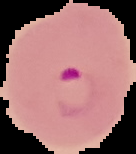

Summary:
  - Image size: 136×154 pixels
  - Result: Plasmodium parasites identified
  - Preparation: thin blood film
  - Image type: cell region segmented out of the field of view; surrounding area masked to black